Locate the red blood cells and classify each one as P. falciparum-infected, uninfected, or of indeterminate infection status.
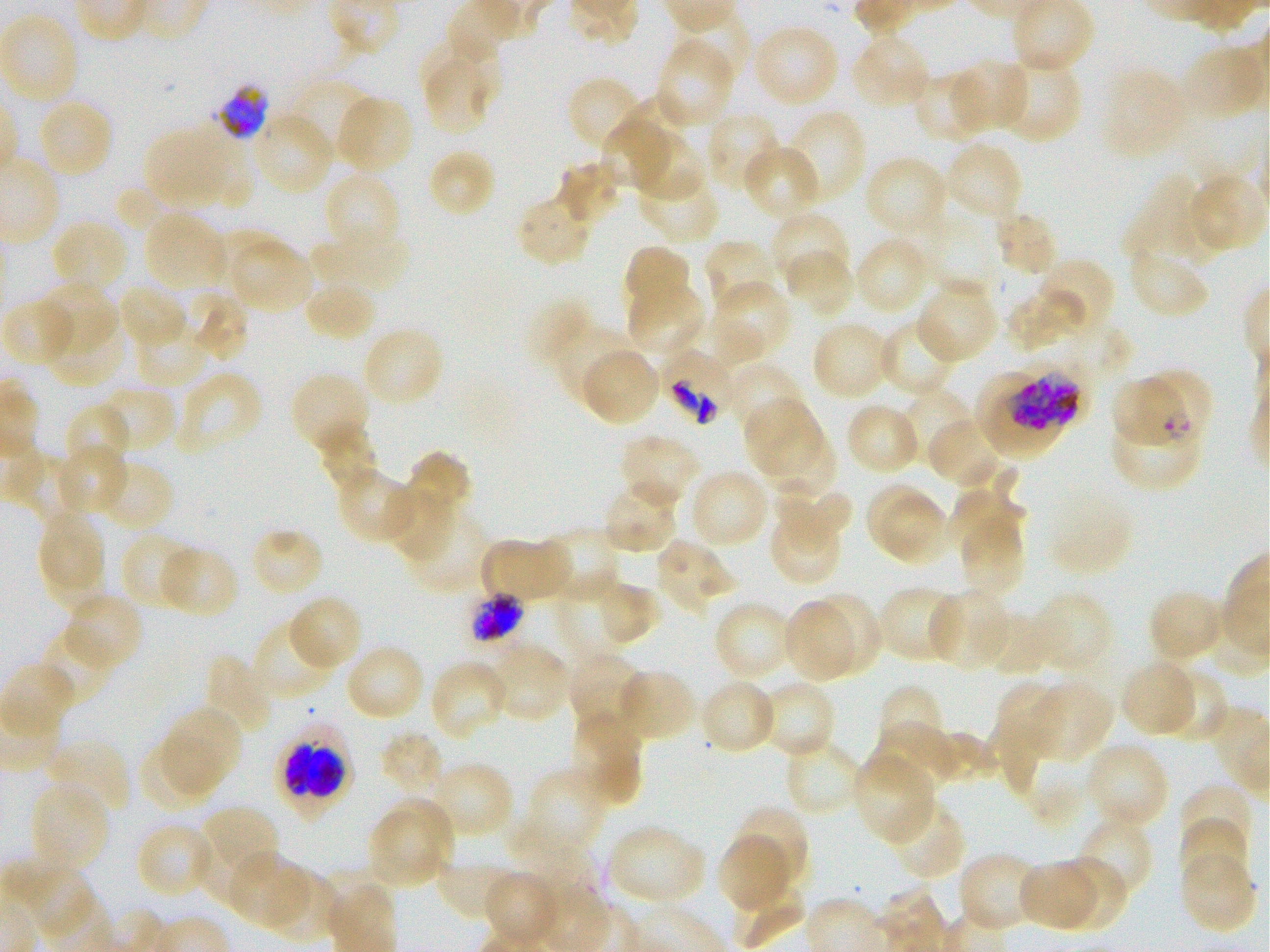
Approximate bounding boxes as {x1, y1, x2, y2} in pixels. Not every red blood cell is marked. A life-cycle stage — or a range of stages, where the recorded stages span more than one — follows each staged infected red blood cell.
Infected red blood cells: {662, 351, 735, 426}; {978, 367, 1078, 459} late trophozoite to late schizont; {1110, 370, 1184, 449}; {1141, 372, 1215, 443} ring; {1110, 413, 1203, 494}; {274, 720, 355, 821}.
Red blood cells of indeterminate infection status: {217, 84, 269, 141}, {467, 592, 525, 643}.
Uninfected red blood cells: {0, 14, 80, 105}, {753, 23, 840, 107}, {851, 34, 931, 109}, {655, 37, 735, 128}, {1181, 45, 1267, 121}, {421, 54, 492, 136}, {1001, 57, 1083, 145}, {955, 58, 1029, 134}, {1103, 68, 1188, 159}, {911, 70, 990, 142}, {567, 75, 645, 152}, {291, 86, 371, 161}, {618, 94, 686, 157}, {334, 95, 413, 174}, {36, 98, 115, 179}, {786, 109, 867, 206}, {706, 110, 784, 193}, {253, 112, 335, 197}, {602, 120, 669, 187}, {143, 126, 231, 206}, {634, 132, 706, 202}, {944, 141, 1024, 222}, {743, 143, 822, 221}, {426, 148, 496, 217}, {864, 155, 949, 238}, {558, 159, 618, 225}, {637, 167, 720, 243}, {322, 171, 402, 256}, {1188, 173, 1265, 253}, {1124, 175, 1195, 260}, {114, 186, 186, 231}, {1168, 187, 1233, 268}, {515, 193, 593, 267}, {994, 210, 1058, 276}, {145, 212, 226, 290}, {769, 212, 850, 291}, {50, 219, 127, 296}, {923, 220, 999, 297}, {317, 226, 406, 296}, {204, 230, 279, 291}, {855, 237, 932, 315}, {230, 238, 313, 312}, {705, 238, 781, 316}, {307, 240, 369, 294}, {622, 244, 692, 320}, {1128, 247, 1207, 318}, {787, 251, 854, 318}, {1034, 257, 1117, 335}, {36, 280, 116, 352}, {302, 280, 377, 343}, {916, 280, 998, 364}, {714, 282, 791, 360}, {117, 283, 186, 352}, {628, 284, 705, 358}, {182, 288, 249, 362}, {1006, 289, 1085, 353}, {524, 297, 593, 368}, {1, 298, 76, 367}, {701, 316, 766, 366}, {45, 317, 125, 387}, {875, 319, 955, 397}, {135, 320, 209, 386}, {810, 321, 890, 401}, {362, 324, 444, 408}, {553, 326, 637, 404}, {581, 346, 659, 426}, {722, 362, 806, 436}, {175, 371, 264, 457}, {290, 373, 369, 455}, {99, 385, 176, 453}, {902, 386, 974, 463}, {743, 399, 820, 474}, {845, 402, 921, 477}, {63, 403, 132, 474}, {927, 418, 1005, 486}, {316, 428, 379, 494}, {763, 428, 837, 497}, {619, 432, 701, 510}, {54, 444, 130, 517}, {404, 450, 473, 520}, {18, 458, 84, 523}, {96, 458, 173, 532}, {335, 467, 417, 544}, {689, 468, 769, 547}, {602, 480, 680, 555}, {772, 480, 851, 554}, {865, 485, 937, 553}, {383, 486, 453, 560}, {949, 490, 1016, 560}, {881, 496, 953, 569}, {38, 512, 104, 586}, {404, 513, 491, 595}, {768, 513, 842, 587}, {958, 519, 1024, 595}, {539, 526, 620, 603}, {249, 527, 325, 598}, {120, 531, 195, 610}, {480, 537, 571, 604}, {42, 538, 110, 613}, {655, 539, 735, 613}, {159, 545, 240, 619}, {557, 568, 629, 663}, {595, 580, 661, 646}, {876, 586, 961, 664}, {927, 588, 1010, 670}, {1146, 588, 1224, 665}, {1031, 591, 1114, 676}, {64, 592, 143, 671}, {805, 593, 881, 677}, {288, 594, 364, 672}, {781, 600, 856, 685}, {713, 601, 792, 681}, {979, 613, 1054, 677}, {254, 619, 336, 701}, {37, 624, 116, 708}, {344, 643, 424, 721}, {488, 643, 571, 723}, {568, 650, 646, 732}, {203, 652, 274, 736}, {429, 658, 509, 739}, {1119, 661, 1197, 738}, {615, 667, 697, 743}, {1162, 675, 1229, 741}, {1029, 679, 1113, 761}, {705, 680, 774, 749}, {993, 680, 1066, 762}, {759, 684, 835, 757}, {877, 684, 945, 754}, {163, 707, 242, 790}, {571, 713, 643, 807}, {987, 719, 1041, 795}, {872, 720, 950, 794}, {930, 730, 999, 781}, {379, 731, 444, 798}, {45, 737, 132, 816}, {788, 738, 862, 813}, {140, 740, 219, 810}, {1083, 742, 1169, 830}, {855, 753, 937, 842}, {428, 762, 514, 835}, {525, 767, 607, 854}, {29, 782, 111, 875}, {1178, 783, 1253, 852}, {380, 795, 454, 875}, {195, 804, 278, 884}, {733, 804, 810, 888}, {891, 804, 962, 876}, {509, 809, 597, 900}, {369, 813, 436, 887}, {1179, 814, 1250, 890}, {1077, 816, 1155, 899}, {135, 822, 216, 900}, {609, 825, 706, 907}, {192, 828, 264, 904}, {717, 835, 792, 913}, {227, 851, 309, 930}, {1179, 851, 1256, 935}, {957, 852, 1041, 934}, {436, 858, 517, 922}, {1016, 858, 1101, 932}, {1051, 858, 1128, 933}, {266, 867, 340, 943}, {484, 871, 561, 947}, {731, 886, 804, 950}.

100x objective under oil immersion, numerical aperture 1.25. Image is 1270×952 pixels. Static in-vitro culture of P. falciparum strain 3D7. Blood group of the donor: O+. Giemsa stain. Thin blood film. One field from this slide.